Identify the preparation type.
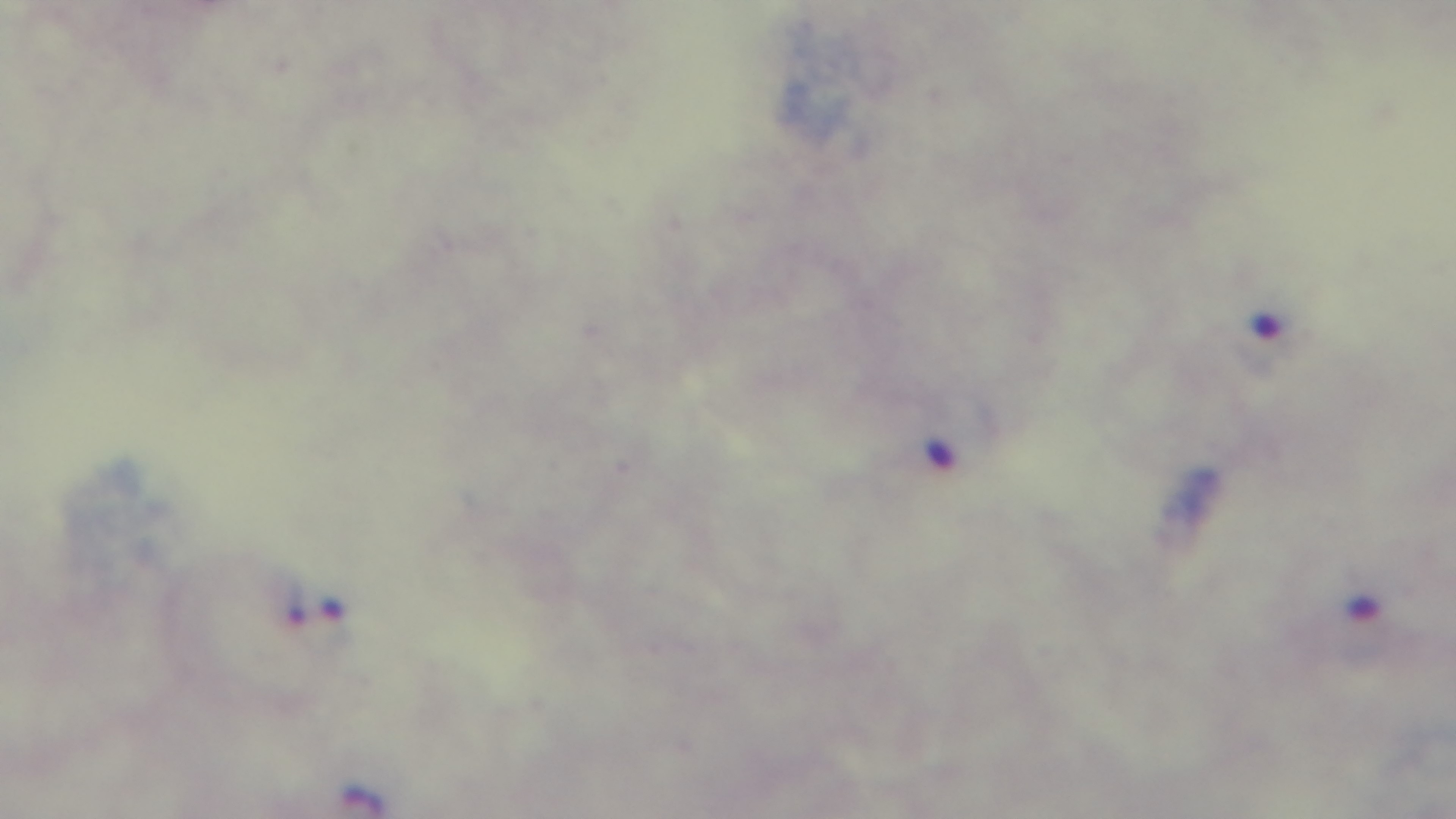

It is a thick blood film.

Oil-immersion objective, 100x. Giemsa stain. Malaria status: infected. Single field of view. Mounted 4K digital camera. Light microscopy.